Locate and identify every blood parasite.
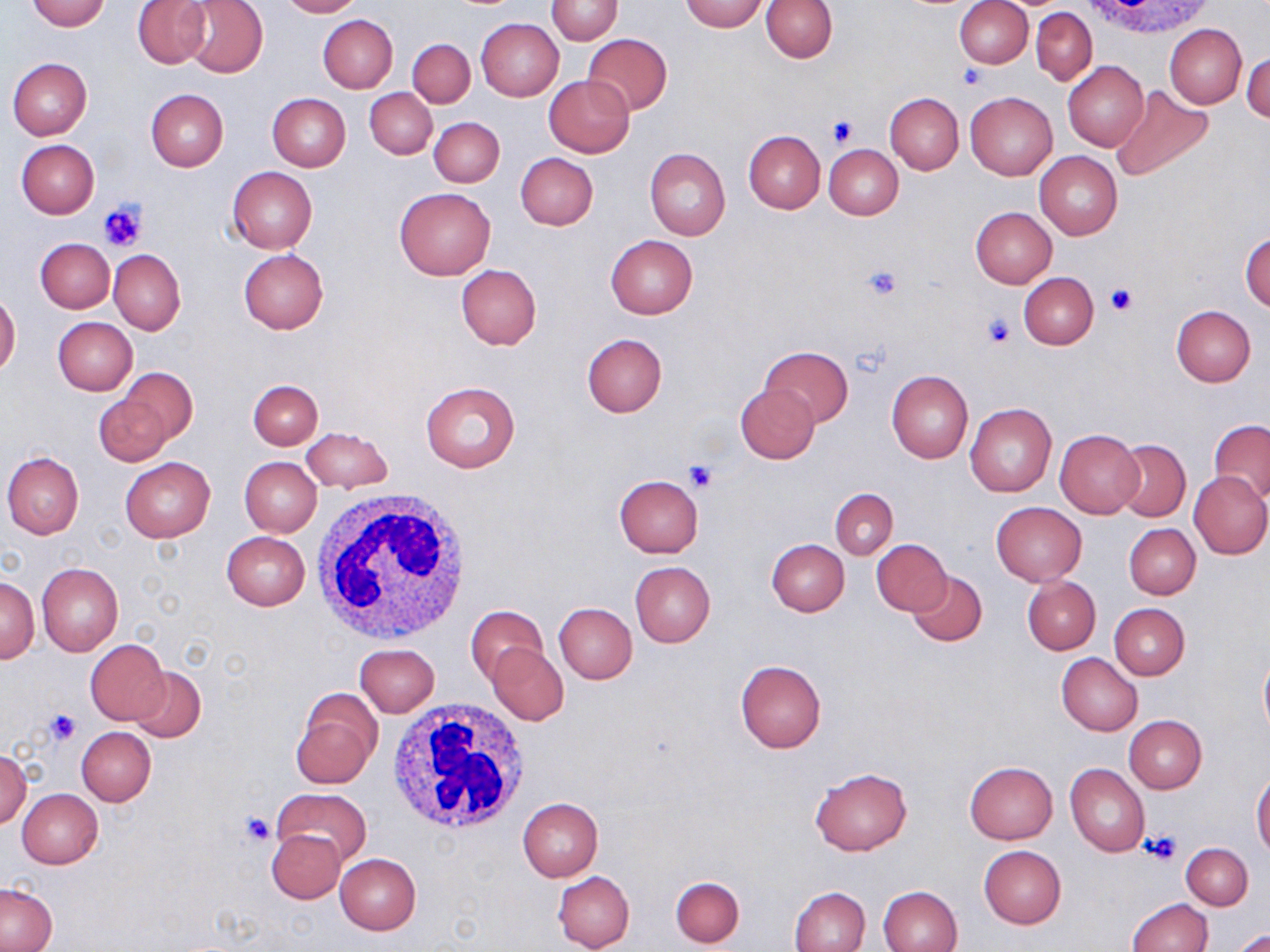
No blood parasites seen.

Approximate bounding boxes as (x1, y1, x2, y2) in pixels. Platelet locations: (959, 64, 987, 89), (827, 114, 860, 147), (99, 201, 147, 252), (864, 263, 904, 301), (1109, 284, 1137, 313), (981, 313, 1016, 350), (684, 461, 718, 494), (45, 708, 80, 746), (239, 810, 275, 846), (1142, 833, 1180, 866). White blood cell locations: (1086, 0, 1215, 41), (312, 485, 473, 643), (387, 703, 529, 838). Uninfected red blood cell locations: (26, 0, 109, 31), (133, 0, 212, 68), (181, 0, 268, 78), (277, 0, 362, 17), (546, 0, 622, 44), (681, 0, 767, 32), (760, 0, 837, 62), (954, 1, 1032, 67), (1031, 7, 1096, 84), (318, 14, 398, 93), (475, 19, 563, 101), (1164, 23, 1247, 109), (582, 33, 672, 115), (408, 39, 475, 108), (1243, 51, 1269, 125), (7, 58, 92, 139), (1063, 61, 1149, 152), (544, 75, 635, 157), (1112, 85, 1214, 182), (365, 89, 437, 158), (146, 90, 228, 170), (966, 91, 1058, 181), (267, 92, 351, 170), (884, 92, 964, 175), (428, 118, 503, 187), (742, 129, 825, 213), (16, 139, 99, 218), (824, 145, 903, 220), (645, 147, 730, 241), (1035, 151, 1122, 240), (515, 152, 599, 229), (227, 167, 317, 254), (394, 187, 495, 280), (969, 207, 1056, 288), (1241, 231, 1269, 314), (605, 235, 698, 319), (36, 238, 114, 313), (238, 248, 328, 334), (108, 249, 185, 335), (455, 264, 542, 350), (1019, 272, 1098, 349), (0, 292, 21, 376), (1170, 305, 1255, 386), (53, 317, 138, 396), (580, 333, 667, 418), (759, 345, 852, 429), (118, 367, 198, 446), (886, 370, 973, 462), (248, 380, 322, 449), (421, 381, 521, 472), (735, 382, 819, 463), (94, 396, 170, 467), (964, 402, 1057, 497), (1210, 420, 1270, 504), (301, 427, 392, 493), (1055, 430, 1143, 517), (1113, 438, 1191, 521), (2, 452, 84, 538), (120, 457, 214, 542), (240, 457, 321, 536), (1188, 471, 1270, 558), (614, 474, 704, 557), (830, 488, 897, 561), (991, 502, 1087, 586), (1124, 524, 1201, 599), (221, 531, 310, 610), (766, 538, 849, 616), (870, 538, 952, 615), (630, 561, 715, 647), (38, 562, 123, 656), (907, 569, 988, 647), (1022, 575, 1101, 655), (1, 576, 39, 664), (554, 602, 637, 683), (1108, 602, 1190, 680), (466, 606, 548, 686), (85, 640, 169, 724), (488, 643, 568, 726), (354, 644, 440, 717), (1258, 649, 1270, 746), (1057, 653, 1142, 735), (734, 660, 827, 754), (128, 665, 207, 743), (292, 689, 381, 789), (1122, 715, 1207, 794), (76, 727, 156, 806), (0, 749, 31, 829), (965, 761, 1057, 843), (1066, 764, 1149, 858), (810, 767, 912, 856), (1251, 772, 1270, 856), (272, 788, 372, 866), (18, 789, 103, 868), (517, 796, 603, 881), (266, 829, 345, 904), (1181, 843, 1252, 910), (979, 845, 1065, 928), (335, 853, 421, 934), (552, 870, 635, 952), (670, 875, 745, 947), (0, 884, 57, 951), (789, 885, 869, 952), (878, 885, 963, 951), (1128, 897, 1213, 951), (1231, 928, 1270, 951). Slide-level diagnosis: negative for blood parasites. May-Grünwald-Giemsa stain. Thin blood smear. Single field of view. Optical microscopy. Image is 1270×952 pixels. 1000x magnification.